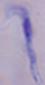

A trypanosome is shown. Micrograph. 1000x magnification.